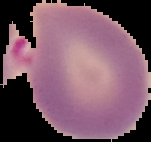 Result: Plasmodium parasites identified. From a thin blood film. Image is 151×142 pixels. The area outside the segmented cell region is set to black.